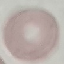
result = no malaria parasites detected
capture = smartphone camera at the microscope eyepiece
preparation = thin blood smear
image type = cell patch, automatically extracted from a larger field of view and resized to 64 × 64 pixels
stain = Giemsa